State which parasite is depicted.
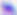

Toxoplasma gondii.

Summary:
  - Modality: micrograph
  - Magnification: 400x